Assess this cell for malaria.
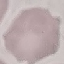

Uninfected.

Summary:
  - Capture: smartphone camera at the microscope eyepiece
  - Image type: automatically extracted cell patch, resized to 64 × 64 pixels
  - Stain: Giemsa
  - Preparation: thin smear